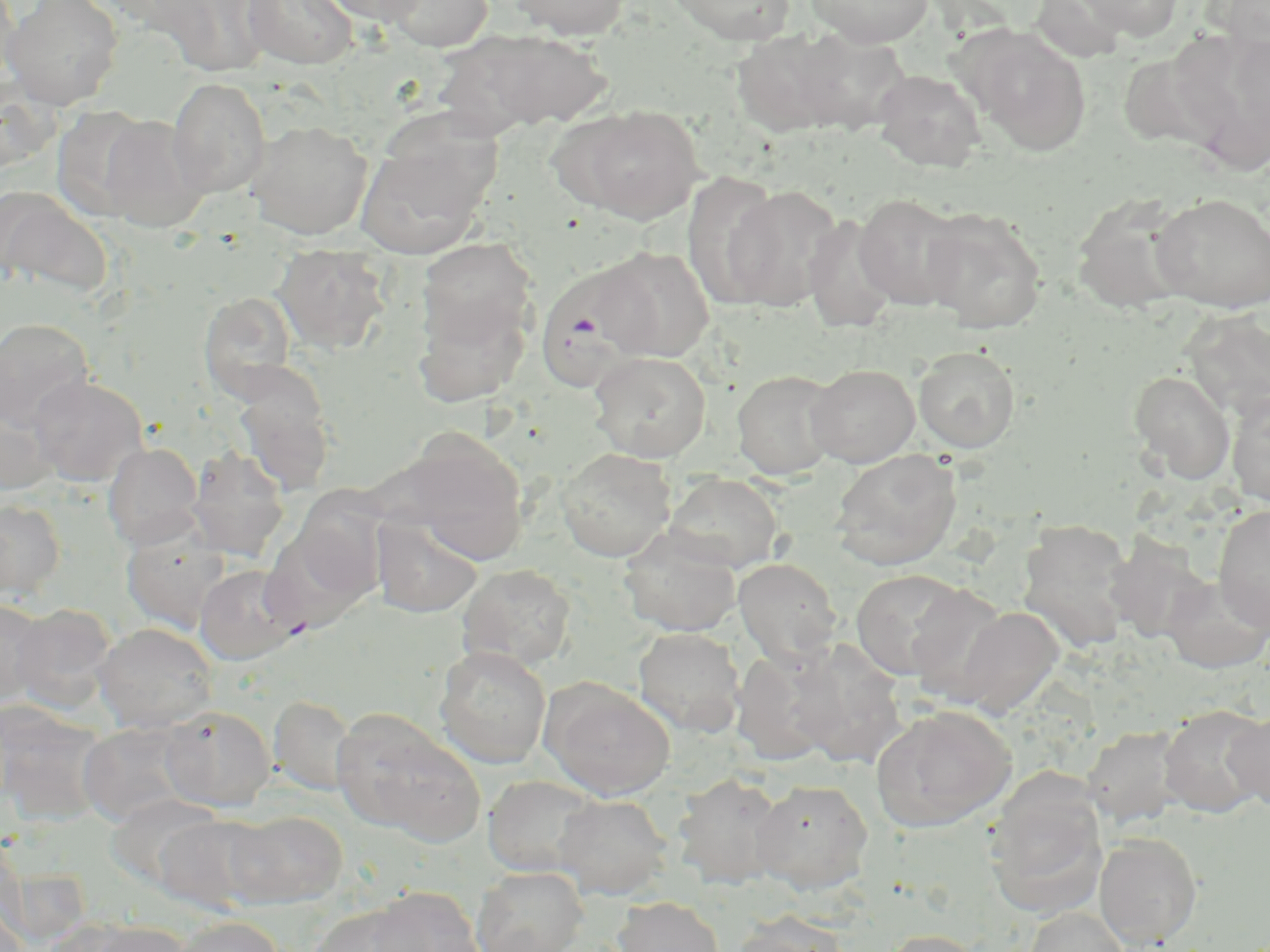
slide_level_diagnosis: Plasmodium falciparum
stain: May-Grünwald-Giemsa
plasmodium_falciparum_infected_red_blood_cell_locations: 'approximate bounding boxes as (x1,y1)-(x2,y2) corner pairs in pixels: (533,263)-(658,393)'
uninfected_red_blood_cell_locations: 'approximate bounding boxes as (x1,y1)-(x2,y2) corner pairs in pixels: (0,0)-(20,89), (2,0)-(124,110), (150,0)-(275,77), (241,0)-(358,69), (317,0)-(430,26), (384,0)-(492,52), (505,0)-(633,40), (663,0)-(798,46), (804,0)-(934,47), (1070,0)-(1184,41), (723,26)-(844,149), (788,28)-(911,135), (967,28)-(1093,156), (457,29)-(613,131), (1229,33)-(1270,146), (1117,51)-(1226,153), (872,68)-(987,173), (167,78)-(271,197), (568,104)-(704,224), (51,105)-(157,221), (97,114)-(209,231), (245,119)-(372,239), (357,123)-(499,260), (720,181)-(844,311), (0,189)-(111,296), (853,192)-(968,311), (1150,192)-(1270,313), (1070,194)-(1196,316), (920,208)-(1047,334), (802,214)-(898,334), (415,237)-(537,352), (272,243)-(392,355), (593,246)-(714,362), (412,291)-(531,406), (198,292)-(298,401), (1180,307)-(1270,421), (0,318)-(94,431), (913,346)-(1020,453), (588,351)-(712,462), (806,364)-(920,467), (732,369)-(842,480), (1128,370)-(1235,484), (233,371)-(336,496), (29,375)-(148,486), (1224,388)-(1270,507), (0,402)-(55,495), (392,432)-(530,564), (103,442)-(204,549), (186,447)-(290,562), (556,448)-(676,562), (830,449)-(962,571), (663,473)-(785,573), (0,500)-(66,600), (1212,504)-(1270,633), (372,516)-(484,617), (1014,518)-(1137,651), (121,522)-(230,632), (260,527)-(374,636), (618,528)-(741,637), (1105,533)-(1212,644), (732,558)-(843,667), (195,564)-(302,664), (457,564)-(578,670), (849,568)-(977,682), (1159,575)-(1270,674), (903,583)-(1015,704), (0,599)-(48,708), (10,604)-(117,714), (952,606)-(1065,718), (94,622)-(217,733), (633,627)-(746,736), (786,640)-(908,769), (434,645)-(552,768), (731,645)-(845,766), (541,679)-(677,800), (269,695)-(356,795), (870,704)-(1016,832), (160,705)-(275,812), (1158,705)-(1268,817), (0,708)-(108,828), (1223,709)-(1270,812), (333,710)-(483,843), (78,722)-(192,826), (1083,726)-(1187,828), (672,773)-(789,890), (482,775)-(601,877), (985,776)-(1107,918), (750,779)-(874,893), (107,793)-(222,891), (553,793)-(673,900), (225,810)-(347,908), (154,814)-(276,916), (1094,833)-(1203,949), (472,866)-(589,952), (364,886)-(483,952), (613,896)-(725,952), (0,900)-(30,952), (305,904)-(425,952), (1023,905)-(1131,952), (729,914)-(853,952), (171,916)-(285,952), (74,919)-(193,952), (877,929)-(990,952)'
modality: optical microscopy
preparation: thin blood smear
image_size: 1270×952 pixels
magnification: 1000x
field_of_view: single